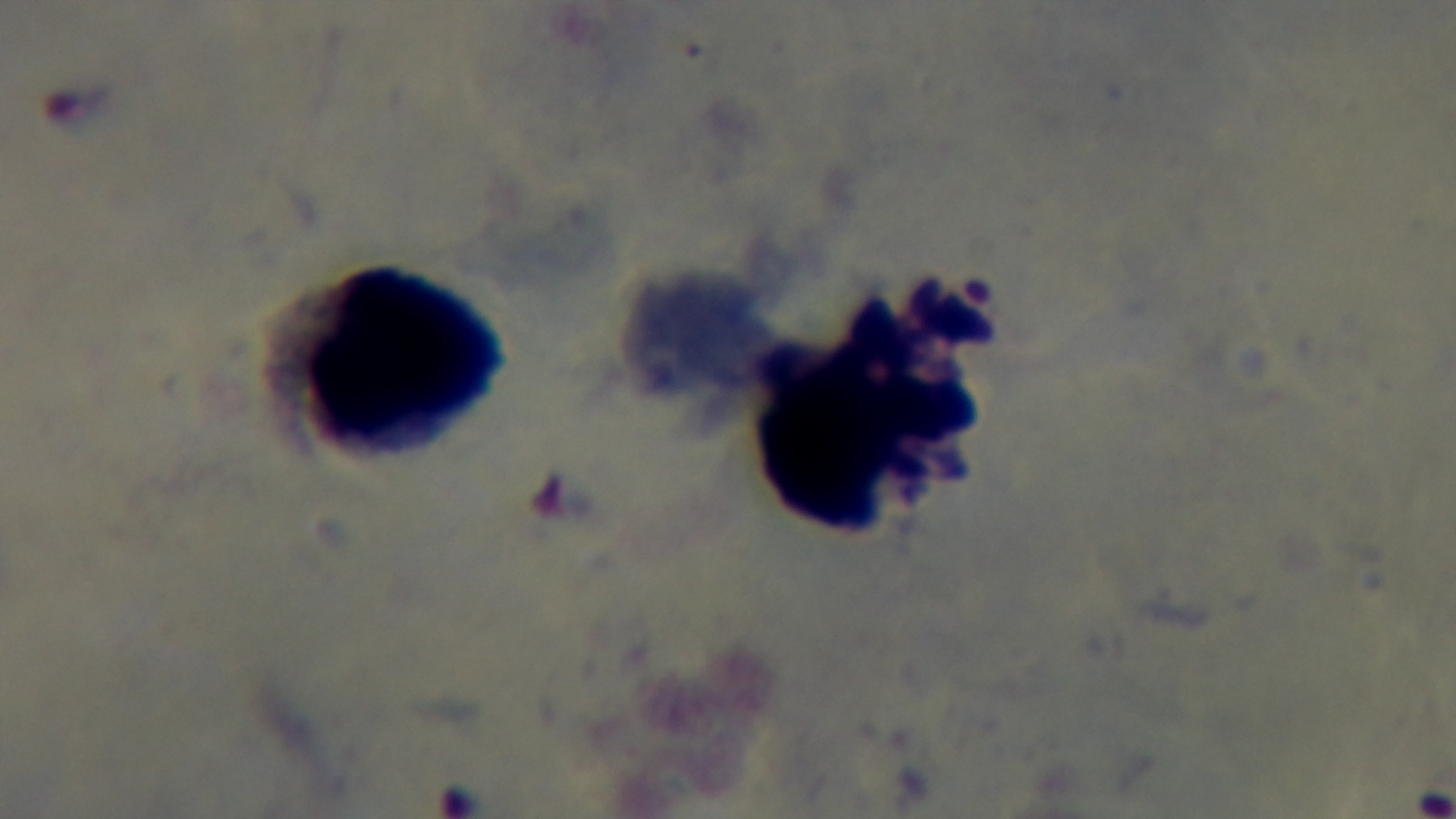
Malaria status: infected. Captured with a mounted 4K digital camera. 100x oil-immersion objective. Light microscopy. One field from the slide. Giemsa-stained. Preparation: thick.